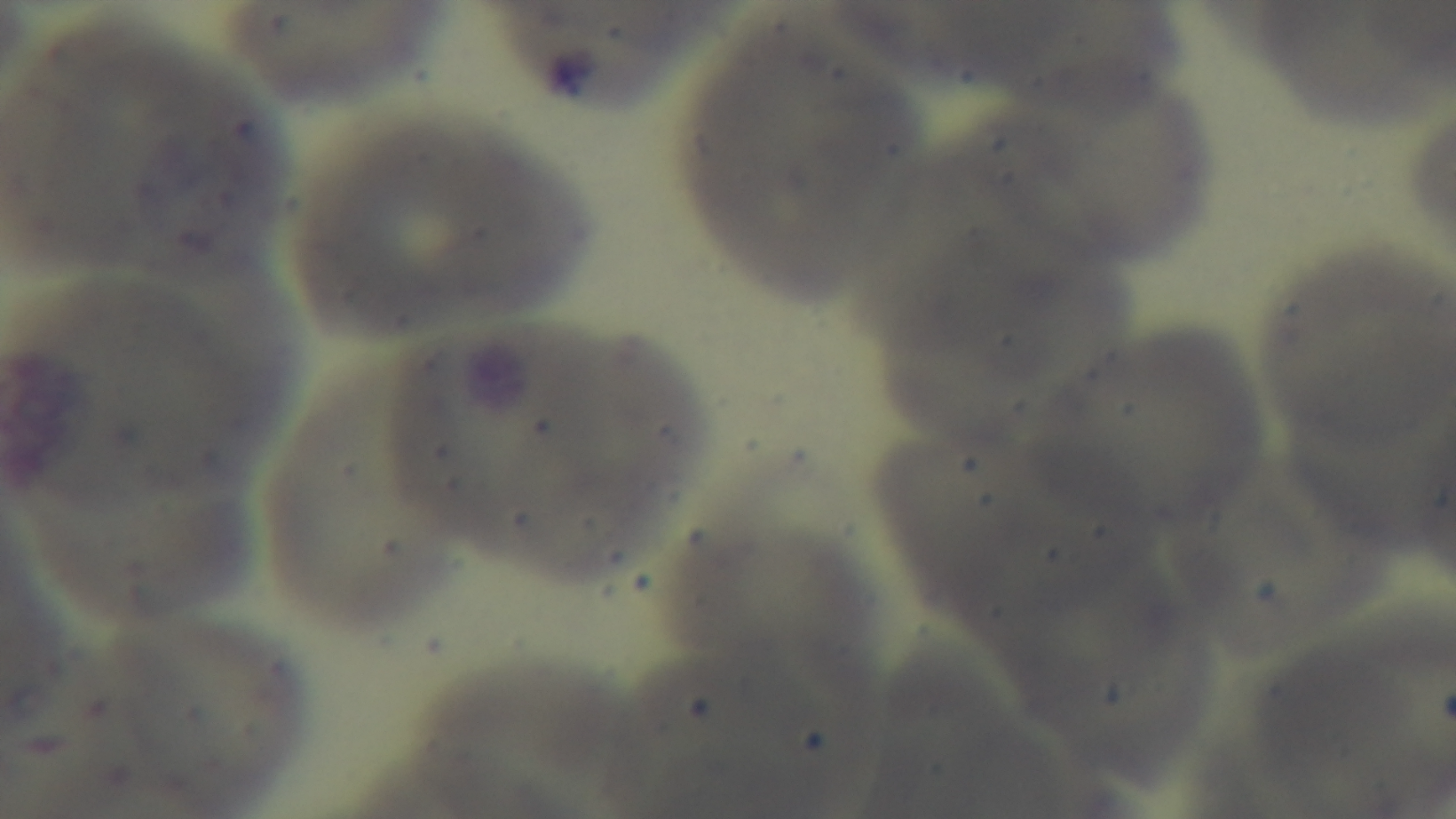 Preparation: thin blood film. Malaria status: negative. Photomicrograph. Oil-immersion objective, 100x. Mounted 4K digital camera. One field from the slide. Giemsa-stained.